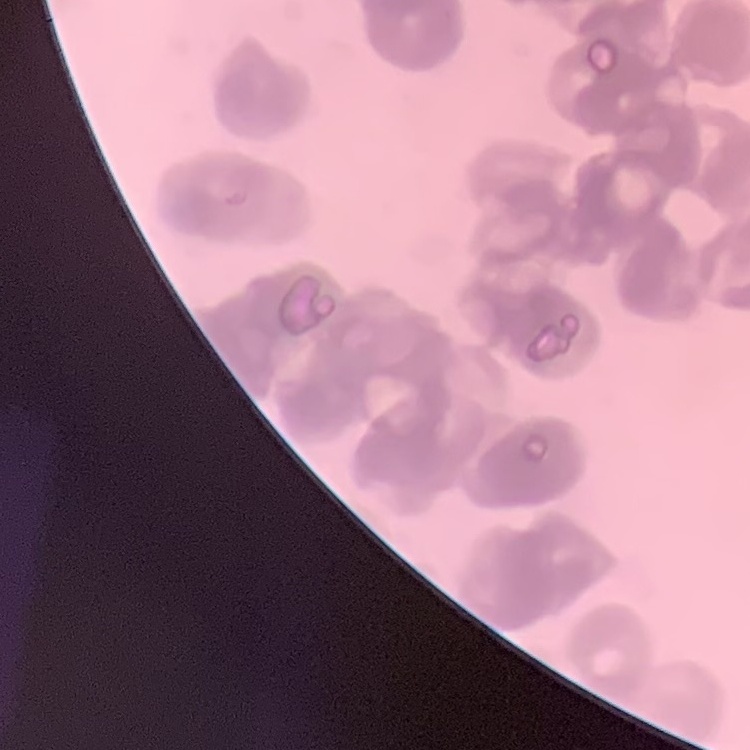

Summary:
  - Red blood cell morphology: rouleaux formation
  - Stain: Field's or Giemsa
  - Image type: square crop of a larger photomicrograph
  - Preparation: thin blood film